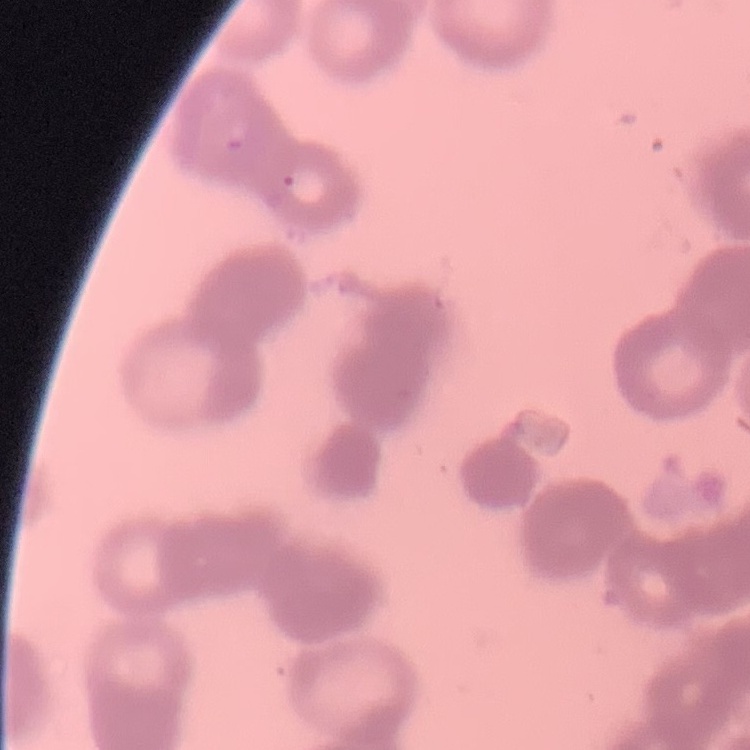

erythrocyte morphology = rouleaux formation
preparation = thin peripheral smear
image type = square crop of a larger photomicrograph
stain = Field's or Giemsa